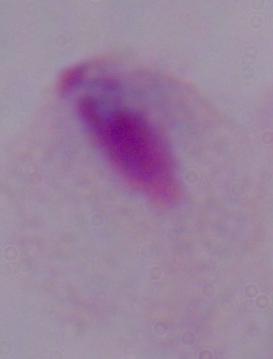

Micrograph. A trichomonad is shown. 1000x magnification.